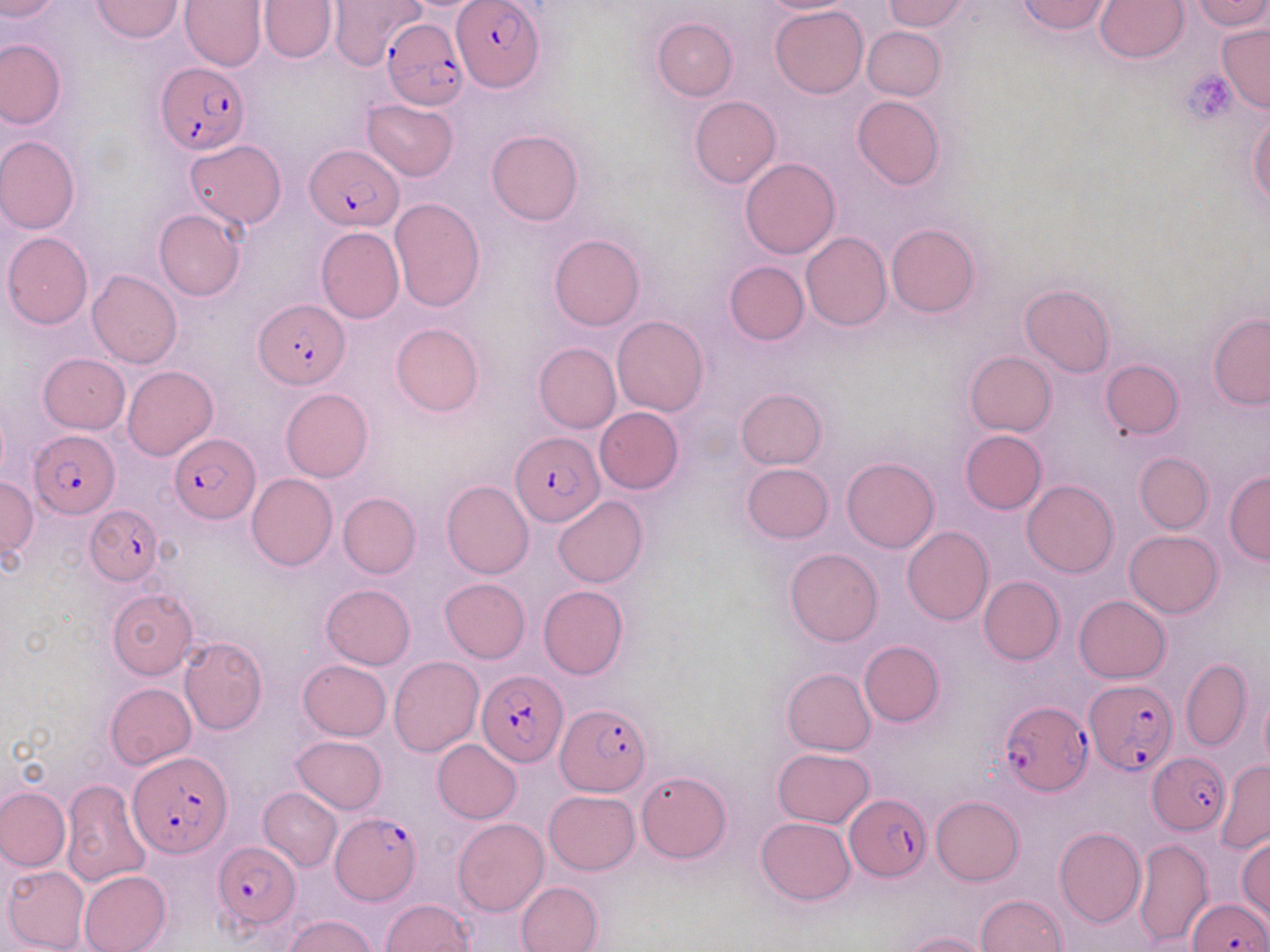
slide-level diagnosis = Plasmodium falciparum
uninfected red blood cell locations = approximate bounding boxes as [x1, y1, x2, y2] in pixels: [0, 0, 59, 20], [91, 0, 183, 42], [180, 0, 266, 71], [258, 0, 336, 62], [329, 0, 426, 71], [756, 0, 858, 14], [883, 0, 971, 30], [1016, 0, 1115, 35], [1094, 0, 1189, 62], [1190, 0, 1269, 30], [771, 6, 868, 98], [651, 18, 737, 101], [1217, 23, 1270, 111], [862, 25, 946, 100], [0, 37, 66, 129], [689, 94, 780, 186], [852, 94, 944, 190], [362, 99, 458, 181], [1249, 115, 1269, 209], [487, 129, 583, 225], [0, 136, 81, 234], [183, 139, 285, 230], [740, 158, 840, 259], [389, 197, 486, 313], [153, 208, 246, 302], [886, 222, 981, 317], [316, 227, 404, 323], [3, 232, 93, 329], [800, 232, 892, 331], [548, 233, 645, 331], [724, 260, 809, 344], [87, 269, 182, 370], [1019, 283, 1114, 377], [1208, 313, 1270, 409], [612, 315, 708, 417], [391, 323, 484, 416], [533, 341, 621, 433], [964, 351, 1057, 436], [38, 353, 129, 433], [1100, 360, 1183, 439], [122, 365, 217, 461], [280, 387, 374, 482], [736, 387, 826, 469], [594, 406, 683, 495], [960, 430, 1047, 514], [1134, 453, 1211, 533], [842, 457, 939, 552], [741, 463, 834, 543], [1223, 471, 1270, 564], [246, 473, 337, 571], [0, 477, 38, 556], [441, 480, 534, 579], [1022, 480, 1118, 577], [338, 492, 420, 578], [553, 497, 647, 588], [902, 527, 994, 625], [1124, 530, 1223, 617], [785, 547, 883, 646], [978, 575, 1064, 664], [440, 577, 530, 662], [320, 585, 415, 669], [538, 585, 629, 678], [107, 589, 198, 679], [1074, 595, 1170, 683], [179, 636, 268, 734], [859, 640, 944, 726], [389, 655, 484, 756], [1181, 658, 1252, 751], [298, 659, 392, 741], [783, 667, 876, 755], [105, 682, 196, 769], [1259, 690, 1270, 769], [290, 735, 386, 813], [432, 740, 522, 823], [771, 748, 875, 828], [1216, 758, 1270, 854], [636, 770, 731, 862], [63, 779, 150, 886], [0, 787, 70, 871], [259, 787, 341, 871], [543, 790, 640, 874], [930, 795, 1024, 886], [755, 816, 855, 905], [453, 818, 549, 915], [1054, 827, 1145, 927], [1236, 835, 1270, 920], [1133, 837, 1211, 949], [1, 865, 89, 952], [78, 870, 171, 952], [517, 881, 603, 952], [975, 894, 1069, 952], [379, 899, 474, 951], [284, 914, 376, 952], [901, 930, 993, 952]
stain = May-Grünwald-Giemsa
Plasmodium falciparum-infected red blood cell locations = approximate bounding boxes as [x1, y1, x2, y2] in pixels: [453, 2, 544, 92], [381, 18, 468, 110], [156, 63, 249, 154], [305, 144, 404, 231], [254, 298, 348, 389], [30, 429, 120, 517], [510, 432, 601, 528], [170, 435, 260, 523], [86, 507, 165, 585], [477, 671, 565, 769], [1084, 678, 1174, 776], [555, 701, 652, 798], [998, 701, 1092, 795], [128, 753, 229, 857], [1148, 753, 1228, 834], [845, 792, 932, 880], [331, 813, 422, 904], [215, 842, 300, 927], [1188, 896, 1268, 952]
preparation = thin blood smear
modality = light microscopy
platelet locations = approximate bounding boxes as [x1, y1, x2, y2] in pixels: [1182, 70, 1236, 123]
field of view = one of a larger specimen
magnification = 1000x
image size = 1270×952 pixels